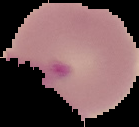

Summary:
  - Image size: 139×127 pixels
  - Preparation: thin blood film
  - Image type: segmented cell region on a black background
  - Result: no Plasmodium parasites seen